Comment on the morphology of the erythrocytes.
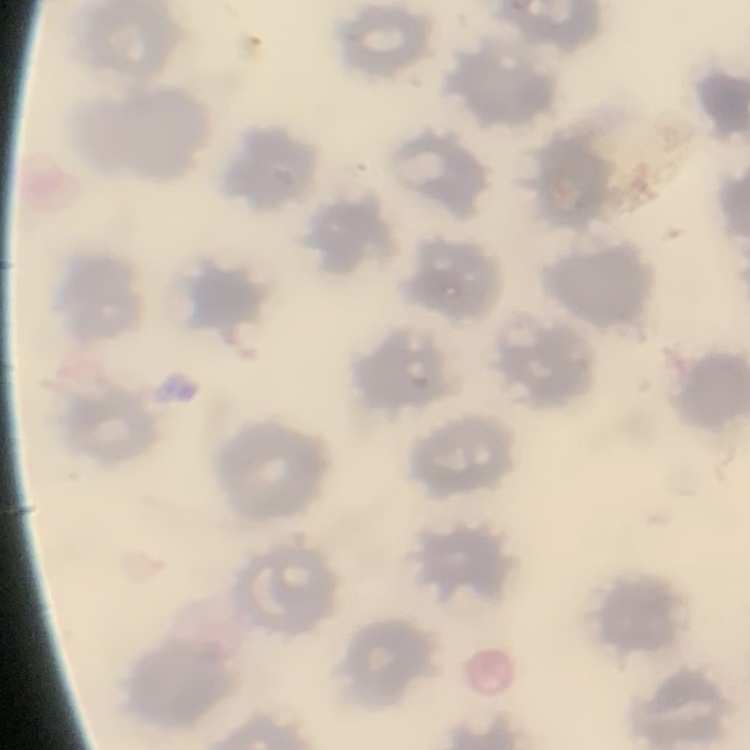

No rouleaux formation.

Field's or Giemsa stain. Thin peripheral smear. One tile cut from a larger photomicrograph.